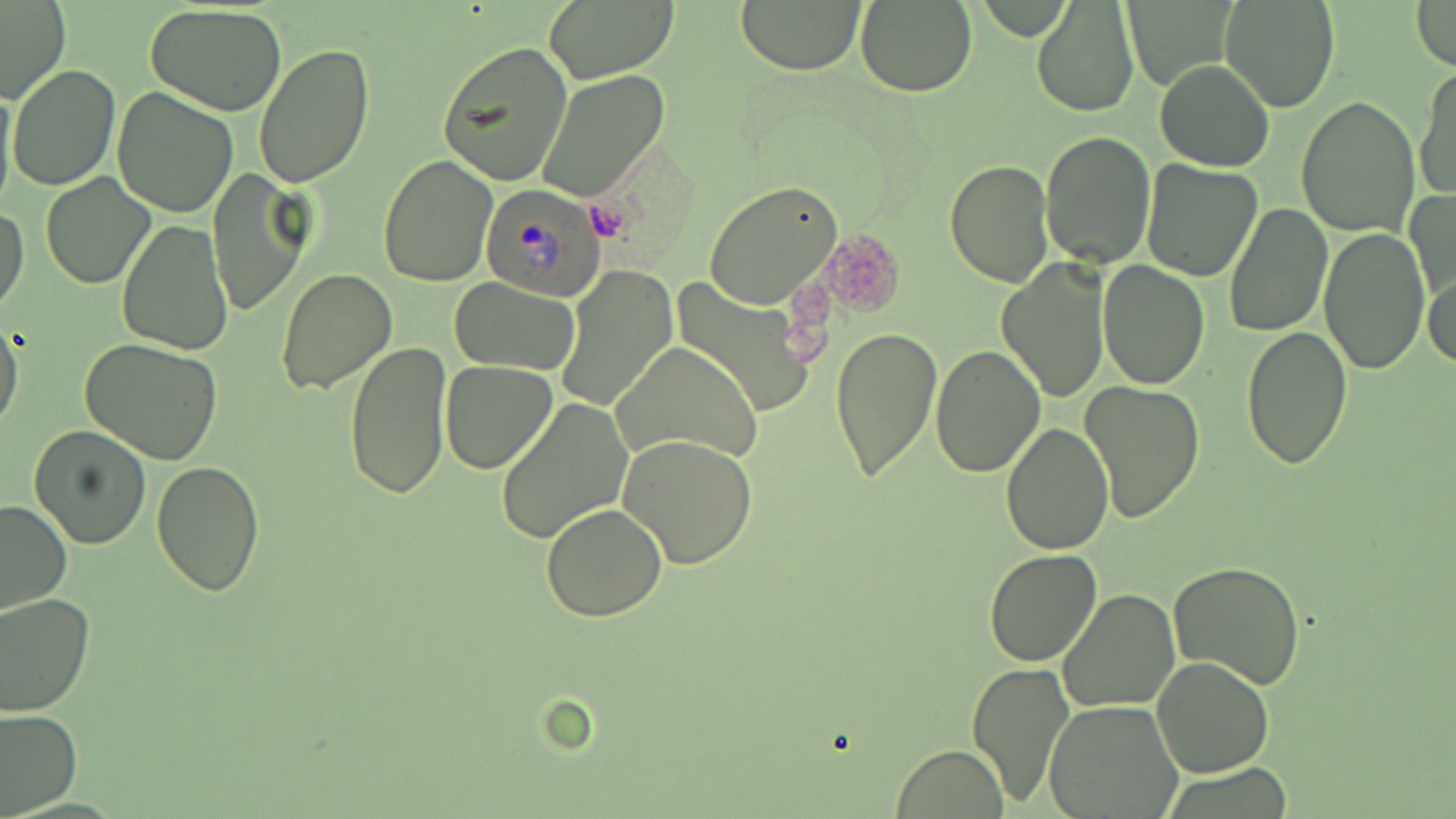

Summary:
  - Coordinate format: approximate bounding boxes as (x1,y1)-(x2,y2) corner pairs in pixels
  - Plasmodium ovale-infected red blood cell locations: (479,183)-(609,300)
  - Platelet locations: (820,231)-(904,314)
  - Uninfected red blood cell locations: (0,0)-(70,104), (540,0)-(678,83), (734,0)-(867,73), (1411,0)-(1456,71), (856,1)-(978,97), (1031,1)-(1140,119), (1221,1)-(1340,112), (144,3)-(289,117), (436,41)-(573,188), (254,43)-(375,189), (1153,59)-(1275,172), (8,65)-(120,191), (1414,66)-(1456,203), (536,70)-(670,201), (7,72)-(236,199), (0,75)-(17,214), (111,86)-(239,218), (1296,95)-(1421,237), (1041,130)-(1156,268), (377,153)-(498,286), (1139,159)-(1265,282), (944,161)-(1052,288), (207,172)-(312,319), (41,173)-(154,289), (703,180)-(841,310), (1406,185)-(1454,317), (1222,203)-(1333,338), (1,205)-(29,317), (116,219)-(234,357), (1318,225)-(1429,373), (996,256)-(1108,400), (1097,259)-(1210,390), (275,266)-(397,396), (557,268)-(677,411), (1424,269)-(1455,374), (668,277)-(816,418), (449,278)-(579,374), (0,319)-(24,437), (830,323)-(941,485), (1241,326)-(1354,470), (80,339)-(225,465), (342,339)-(450,498), (611,342)-(762,467), (930,345)-(1045,477), (440,361)-(557,473), (1080,379)-(1205,522), (495,398)-(634,544), (1002,421)-(1114,554), (27,424)-(153,550), (617,434)-(758,569), (151,461)-(265,596), (0,499)-(75,616), (541,502)-(668,622), (984,547)-(1103,667), (1168,562)-(1306,689), (1059,589)-(1181,714), (0,592)-(96,716), (1151,654)-(1274,777), (968,660)-(1076,806), (1044,699)-(1183,818), (0,706)-(82,815), (891,745)-(1009,819)
  - Slide-level diagnosis: Plasmodium ovale
  - Magnification: 1000x
  - Stain: May-Grünwald-Giemsa
  - Field of view: single
  - Modality: light microscopy
  - Image size: 1456×819 pixels
  - Preparation: thin blood film